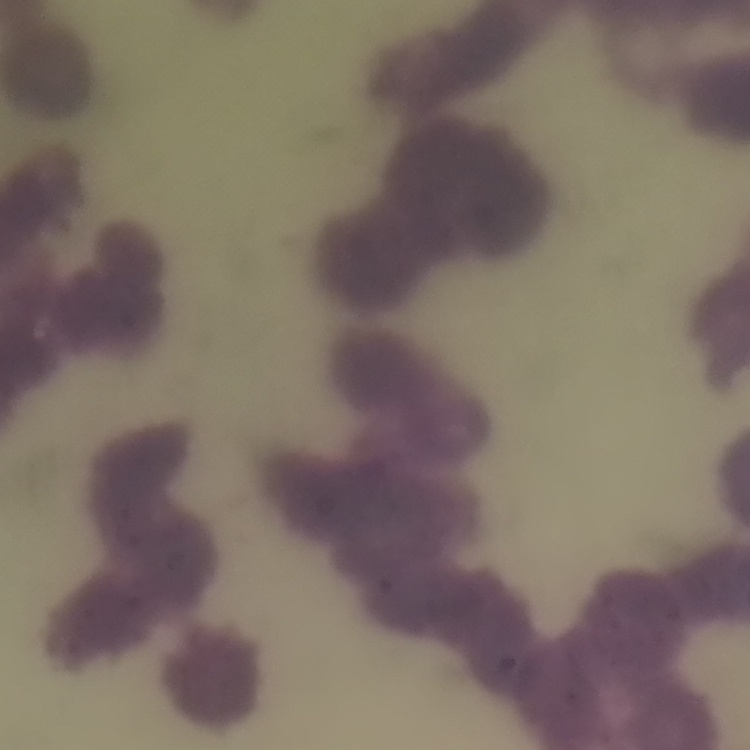

The red blood cells exhibit rouleaux formation. Stained with either Field's or Giemsa. Thin peripheral smear. One tile cut from a larger photomicrograph.